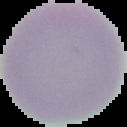 Cell region segmented out of the field of view; the surrounding area is masked to black. From a thin blood smear. Image is 127×127 pixels. Result: no malaria parasites seen.